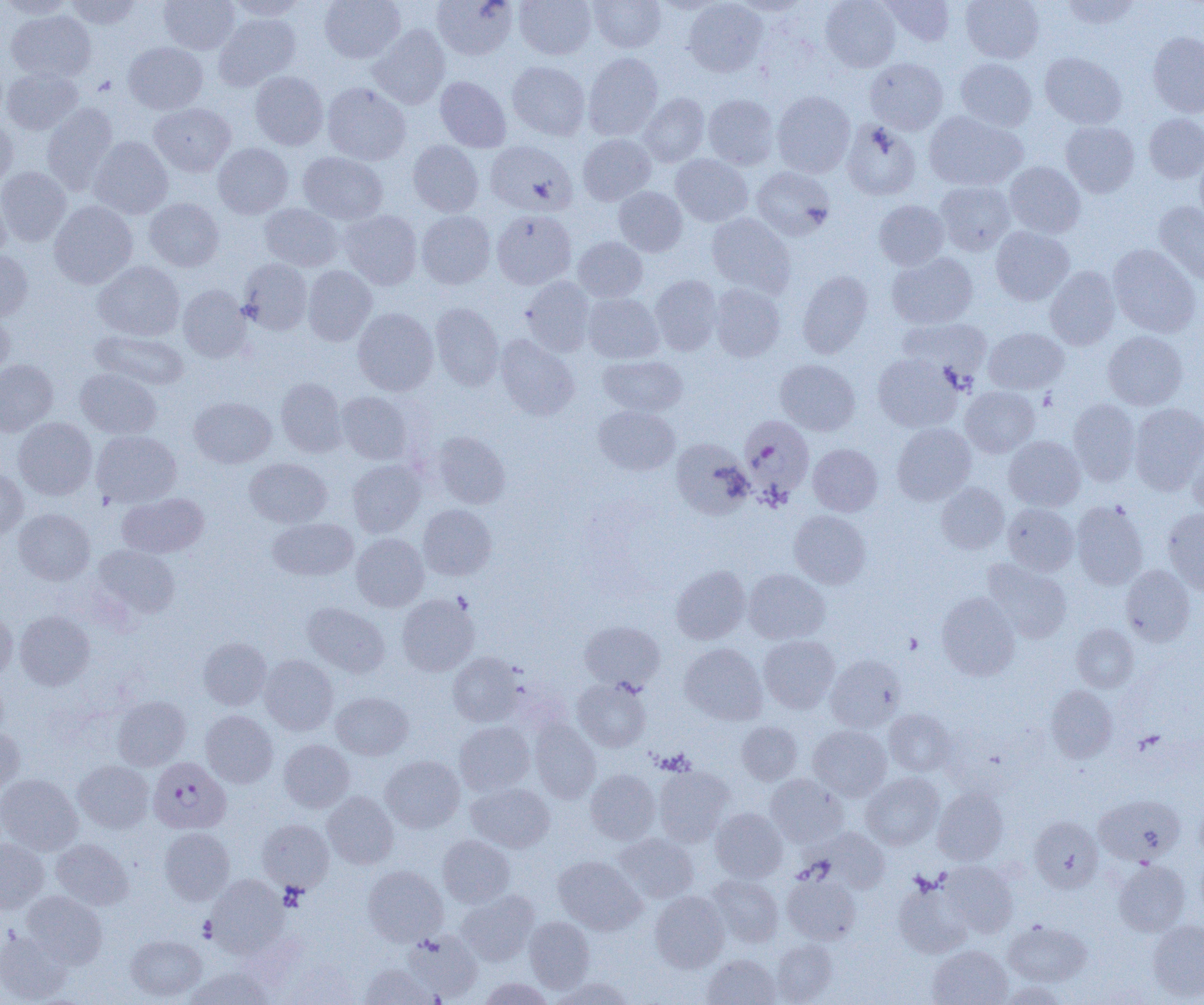

Summary:
  - Coordinate format: approximate bounding boxes as (x1,y1)-(x2,y2) corner pairs in pixels
  - Uninfected red blood cell locations: (0,0)-(76,19), (65,0)-(143,29), (159,0)-(240,54), (227,0)-(309,21), (319,0)-(405,63), (431,0)-(518,60), (514,0)-(596,60), (589,0)-(665,53), (728,0)-(813,16), (820,0)-(901,72), (881,0)-(955,47), (960,0)-(1044,63), (1059,0)-(1142,30), (683,1)-(768,77), (6,10)-(96,82), (213,13)-(301,90), (368,24)-(450,109), (1147,31)-(1204,117), (123,42)-(208,114), (583,52)-(663,140), (1040,52)-(1126,128), (865,58)-(948,134), (955,58)-(1037,131), (507,61)-(590,140), (2,68)-(83,135), (250,71)-(329,150), (435,77)-(511,152), (322,83)-(411,166), (772,90)-(855,178), (639,93)-(710,167), (703,94)-(779,170), (41,103)-(118,194), (149,103)-(236,176), (924,111)-(1027,191), (1143,113)-(1204,183), (0,116)-(17,190), (842,120)-(921,200), (1061,121)-(1139,197), (578,134)-(656,205), (88,136)-(173,219), (485,140)-(577,215), (408,141)-(484,217), (213,143)-(293,218), (1194,148)-(1204,232), (298,151)-(388,224), (671,154)-(753,227), (1004,161)-(1085,238), (0,166)-(71,247), (752,166)-(835,240), (935,180)-(1015,255), (0,186)-(11,262), (613,186)-(687,257), (144,198)-(224,271), (873,199)-(949,270), (49,200)-(138,288), (1154,201)-(1204,285), (259,203)-(343,271), (339,210)-(422,289), (492,210)-(576,289), (416,211)-(496,289), (707,212)-(795,297), (991,226)-(1075,306), (574,237)-(648,302), (1108,244)-(1201,338), (0,250)-(33,321), (887,252)-(978,329), (238,258)-(312,334), (93,261)-(185,341), (1044,265)-(1120,350), (303,266)-(377,346), (797,270)-(873,358), (649,275)-(722,355), (521,276)-(596,356), (709,284)-(785,361), (178,285)-(251,362), (583,293)-(664,363), (430,302)-(504,391), (352,307)-(438,396), (0,309)-(14,382), (897,318)-(991,382), (984,328)-(1069,393), (90,330)-(189,390), (1103,331)-(1188,410), (495,334)-(579,421), (873,353)-(960,432), (598,355)-(688,417), (0,359)-(57,436), (775,359)-(860,436), (75,368)-(162,439), (276,378)-(346,456), (960,386)-(1040,457), (337,392)-(413,464), (189,396)-(276,467), (1068,398)-(1140,486), (1129,403)-(1204,494), (594,405)-(680,475), (13,417)-(97,500), (892,422)-(976,505), (91,430)-(182,507), (433,431)-(510,509), (1004,436)-(1085,511), (672,438)-(753,519), (1187,440)-(1204,518), (809,443)-(883,516), (244,458)-(332,528), (347,460)-(425,537), (0,466)-(28,540), (936,482)-(1009,554), (117,493)-(208,558), (1072,500)-(1148,589), (1003,503)-(1079,575), (418,504)-(497,580), (13,508)-(95,584), (1163,509)-(1204,595), (789,510)-(871,588), (268,517)-(358,580), (351,533)-(429,611), (92,545)-(180,620), (982,559)-(1072,643), (1121,564)-(1195,646), (671,565)-(750,643), (743,569)-(829,644), (397,593)-(479,676), (937,593)-(1020,680), (303,602)-(389,677), (0,609)-(17,681), (15,610)-(95,690), (579,620)-(665,691), (1071,624)-(1138,693), (758,635)-(839,713), (199,637)-(271,710), (681,643)-(767,725), (448,652)-(523,726), (259,654)-(338,735), (826,654)-(905,732), (572,677)-(651,752), (1046,685)-(1117,762), (331,692)-(413,760), (113,696)-(190,770), (884,709)-(955,776), (201,710)-(278,788), (529,718)-(600,804), (455,721)-(534,795), (737,721)-(803,785), (808,725)-(891,801), (0,726)-(25,794), (279,739)-(354,812), (380,755)-(465,833), (74,760)-(154,833), (653,766)-(734,846), (585,769)-(660,844), (861,773)-(944,849), (0,774)-(82,855), (765,774)-(847,847), (466,782)-(554,853), (932,786)-(1008,865), (322,791)-(399,868), (1095,794)-(1184,865), (710,808)-(788,883), (1030,816)-(1103,892), (258,819)-(334,892), (160,827)-(235,905), (816,828)-(890,892), (614,834)-(699,903), (438,835)-(515,907), (51,838)-(132,910), (0,839)-(49,912), (553,855)-(645,934), (941,860)-(1018,937), (1114,860)-(1190,936), (363,865)-(447,946), (782,873)-(861,944), (707,874)-(783,947), (207,875)-(288,956), (893,880)-(973,958), (22,891)-(107,968), (456,891)-(539,966), (650,891)-(730,972), (524,916)-(595,993), (1147,920)-(1204,1000), (1004,921)-(1091,986), (0,930)-(72,1003), (402,931)-(483,1001), (126,934)-(206,1001), (771,938)-(838,1004), (928,945)-(1012,1005), (703,955)-(781,1005), (284,960)-(358,1005), (359,964)-(436,1005), (187,966)-(270,1005), (551,976)-(636,1005), (477,978)-(553,1005), (998,981)-(1068,1005)
  - Platelet locations: (903,632)-(922,654)
  - Plasmodium falciparum-infected red blood cell locations: (739,415)-(814,502), (148,757)-(230,834)
  - Slide-level diagnosis: Plasmodium falciparum
  - Magnification: 1000x
  - Preparation: thin blood smear
  - Modality: light microscopy
  - Image size: 1204×1005 pixels
  - Field of view: single